Report the malaria status of this cell.
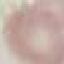
Uninfected.

Photographed with a smartphone camera at the microscope eyepiece. Thin smear of blood. Cell patch, automatically extracted from a larger field of view and resized to 64 × 64 pixels. Giemsa stain.